Point out leukocytes.
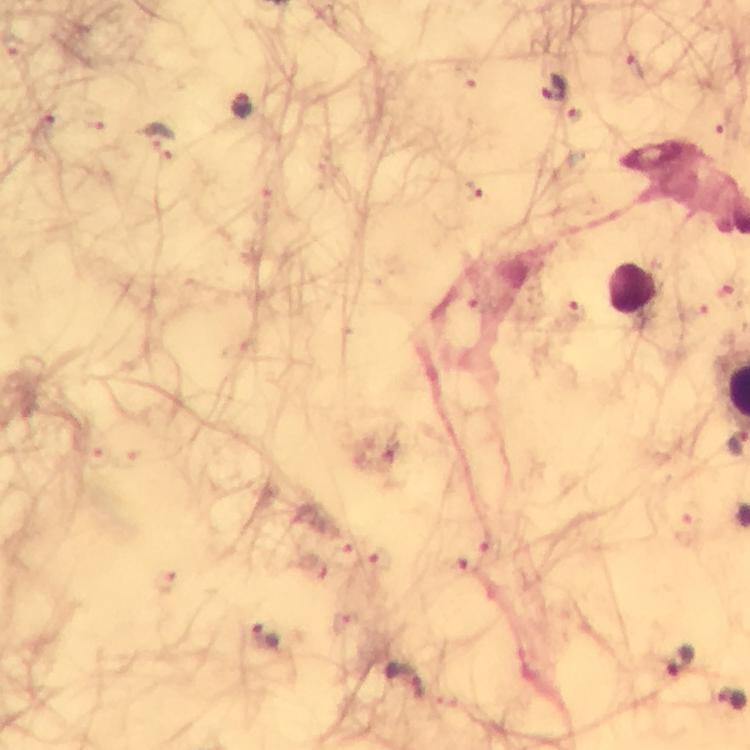
Approximate object centers, in pixels from the top-left corner.
Leukocytes: (x=634, y=289).

preparation = thick blood smear
context = from a malaria diagnostic workup
immersion oil = used
image size = 750×750 pixels
capture = smartphone camera through the microscope
magnification = 100x
stain = Giemsa
malaria parasite locations = approximate object centers, in pixels from the top-left corner: (x=636, y=68), (x=554, y=89), (x=239, y=108), (x=159, y=141), (x=472, y=189), (x=574, y=309), (x=489, y=545), (x=346, y=558), (x=377, y=558), (x=455, y=566), (x=164, y=579), (x=267, y=639), (x=681, y=662), (x=404, y=681)
cropped from = a single field of view